Name the parasite shown.
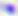
Toxoplasma gondii.

Photomicrograph. Captured at 400x magnification.